Assess this cell for malaria.
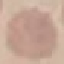

It is uninfected.

capture = smartphone through the microscope eyepiece
preparation = thin blood film
stain = Giemsa
image type = automatically extracted cell patch, resized to 64 × 64 pixels